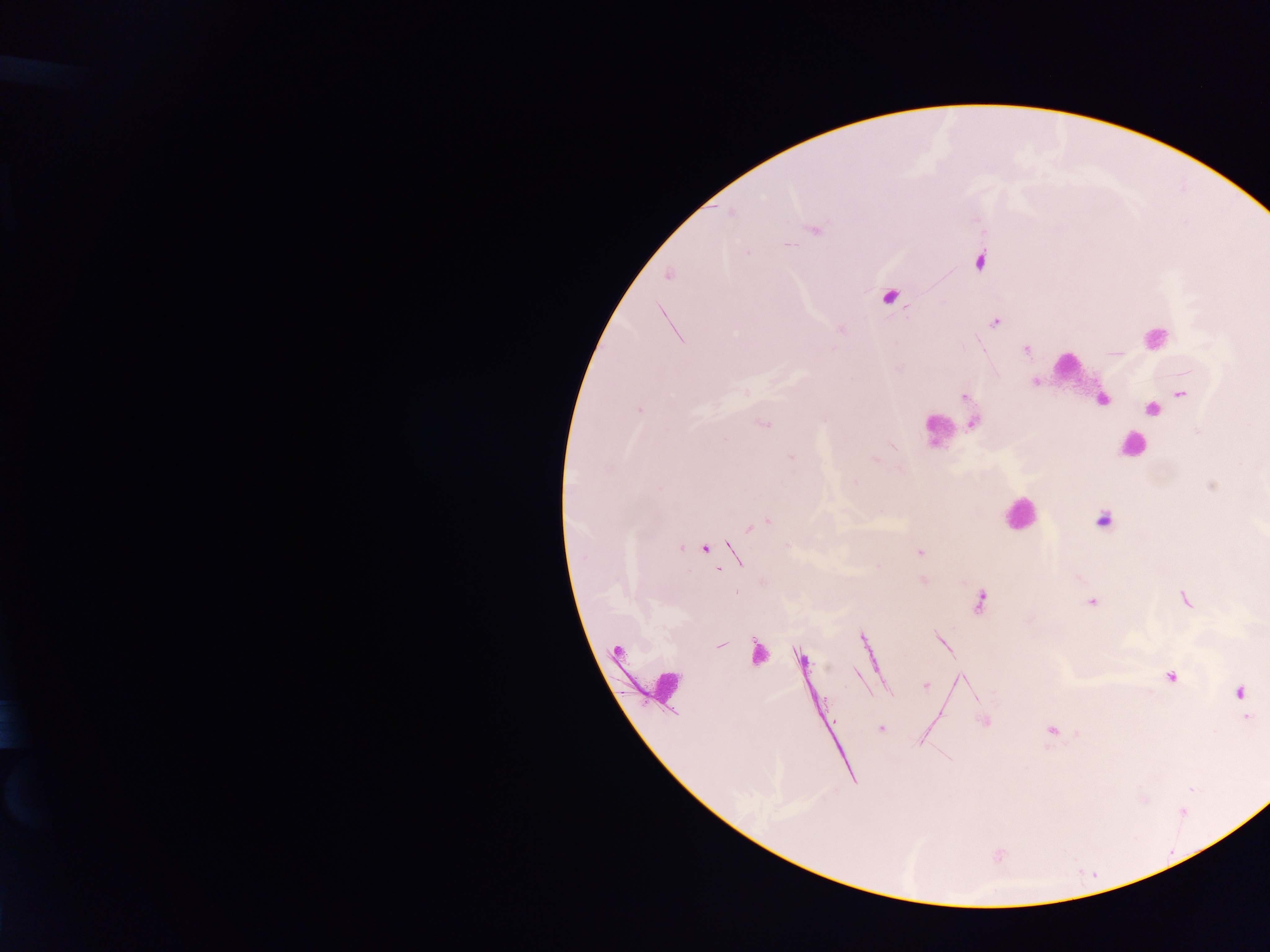

image size = 1270×952 pixels
malaria parasite locations = approximate centers as x y in pixels: 731 213; 815 229; 789 245; 980 261; 668 276; 889 297; 995 323; 1026 349; 1035 382; 1181 394; 964 397; 1102 400; 1152 409; 640 410; 973 423; 763 424; 791 457; 1102 520; 765 521; 757 525; 681 548; 705 549; 919 553; 734 555; 922 579; 736 593; 1184 600; 980 602; 1092 602; 720 644; 757 652; 801 658; 1171 676; 926 686; 1239 692; 1248 717; 984 722; 881 729; 1052 731
leukocyte locations = approximate centers as x y in pixels: 1155 337; 1066 365; 936 428; 1131 445; 1019 513; 664 683
capture = mobile-phone photograph through a microscope
preparation = thick blood film
country = Ghana
field of view = single